Report the malaria status of this cell.
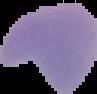
It is uninfected.

{
  "image_type": "segmented cell region with the area outside set to black",
  "image_size": "97×94 pixels",
  "preparation": "thin blood smear"
}